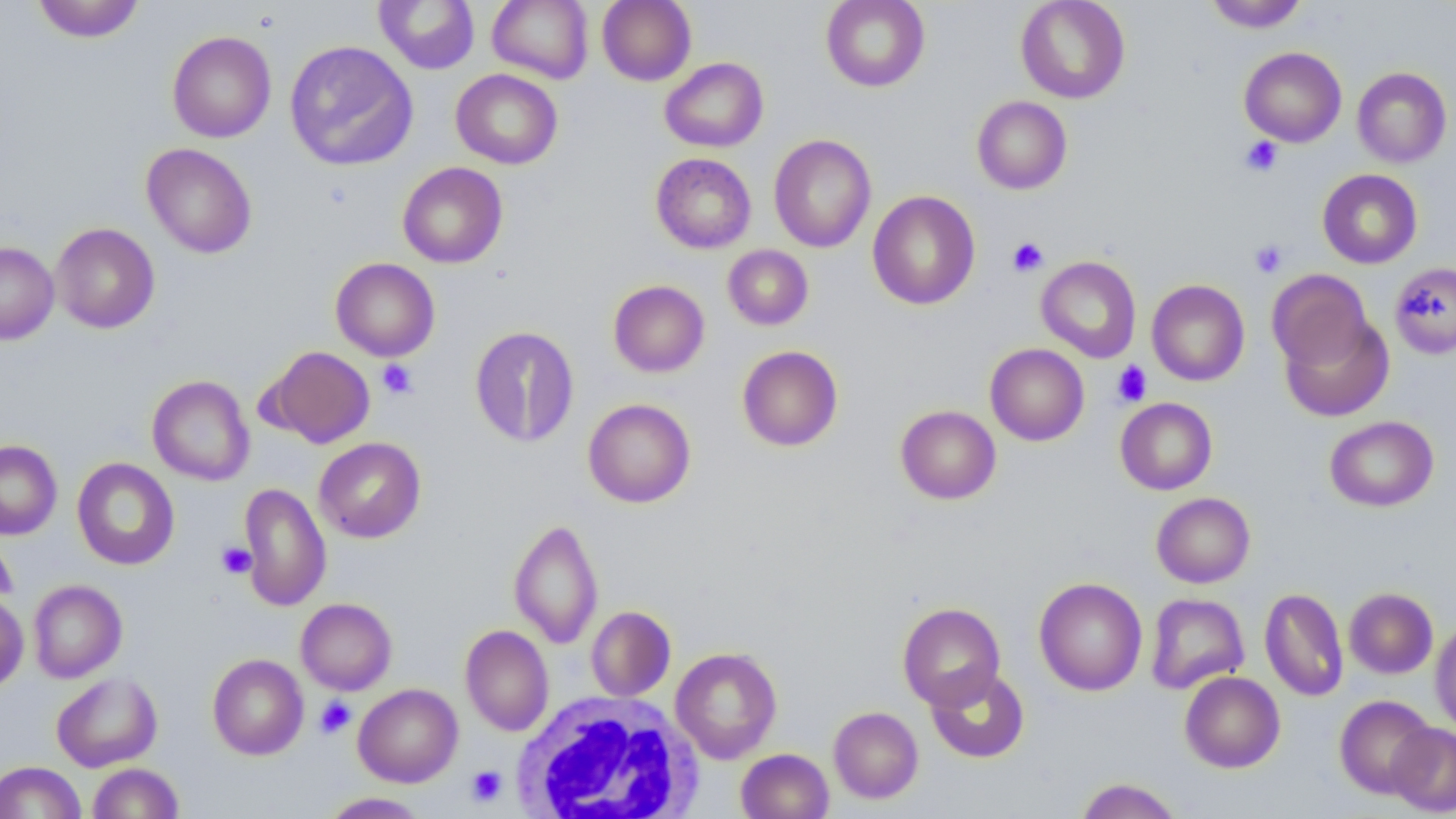
Summary:
  - Coordinate format: approximate bounding boxes as (x1, y1, x2, y2) in pixels
  - Platelet locations: (1240, 136, 1283, 176), (1007, 237, 1049, 277), (1250, 239, 1288, 278), (377, 359, 417, 399), (1112, 360, 1152, 407), (217, 542, 256, 579), (314, 696, 357, 739), (466, 765, 507, 807)
  - Uninfected red blood cell locations: (31, 0, 146, 43), (375, 0, 480, 74), (487, 0, 593, 84), (597, 0, 696, 86), (821, 0, 930, 92), (1015, 0, 1131, 104), (1202, 0, 1309, 33), (167, 30, 276, 143), (284, 40, 418, 172), (1239, 47, 1347, 147), (659, 57, 769, 152), (1352, 67, 1452, 168), (451, 69, 563, 169), (971, 96, 1072, 194), (768, 134, 876, 253), (141, 143, 257, 259), (650, 153, 757, 253), (397, 162, 508, 268), (1317, 169, 1423, 269), (867, 190, 981, 310), (51, 223, 160, 334), (0, 241, 59, 345), (723, 245, 814, 330), (1036, 256, 1141, 363), (330, 258, 440, 361), (1390, 263, 1456, 358), (1267, 270, 1373, 370), (1147, 279, 1250, 386), (608, 280, 709, 377), (1279, 312, 1394, 422), (469, 325, 580, 448), (985, 343, 1090, 446), (737, 345, 843, 452), (263, 346, 375, 448), (147, 374, 254, 485), (583, 398, 696, 508), (1115, 398, 1217, 495), (895, 405, 1001, 505), (1324, 416, 1439, 512), (314, 437, 426, 543), (0, 439, 62, 540), (72, 457, 180, 570), (238, 482, 331, 612), (1151, 492, 1256, 588), (508, 517, 603, 649), (0, 527, 17, 609), (1033, 577, 1148, 696), (28, 579, 127, 683), (1259, 587, 1348, 702), (1344, 587, 1438, 679), (0, 593, 28, 692), (1145, 593, 1249, 694), (296, 598, 397, 695), (897, 602, 1006, 709), (586, 606, 676, 701), (1430, 620, 1456, 736), (460, 625, 554, 736), (670, 647, 783, 763), (207, 653, 308, 760), (925, 667, 1030, 764), (1179, 671, 1285, 773), (51, 672, 163, 772), (353, 683, 463, 787), (1334, 695, 1437, 799), (829, 706, 924, 804), (1387, 723, 1456, 816), (736, 748, 833, 819), (0, 761, 86, 819), (87, 763, 184, 819), (1075, 778, 1184, 819), (319, 792, 429, 818)
  - White blood cell locations: (510, 690, 704, 818)
  - Slide-level diagnosis: negative for blood parasites
  - Modality: optical microscopy
  - Image size: 1456×819 pixels
  - Field of view: one of a larger specimen
  - Stain: May-Grünwald-Giemsa
  - Magnification: 1000x
  - Preparation: thin blood smear